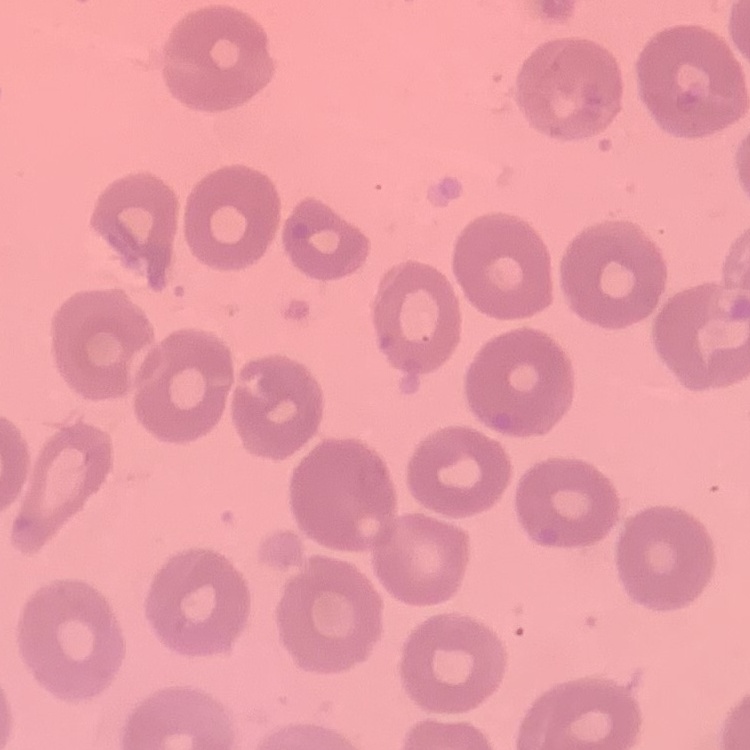
Summary:
  - Red blood cell morphology: no rouleaux formation
  - Image type: one tile cut from a larger photomicrograph
  - Preparation: thin blood film
  - Stain: Field's or Giemsa